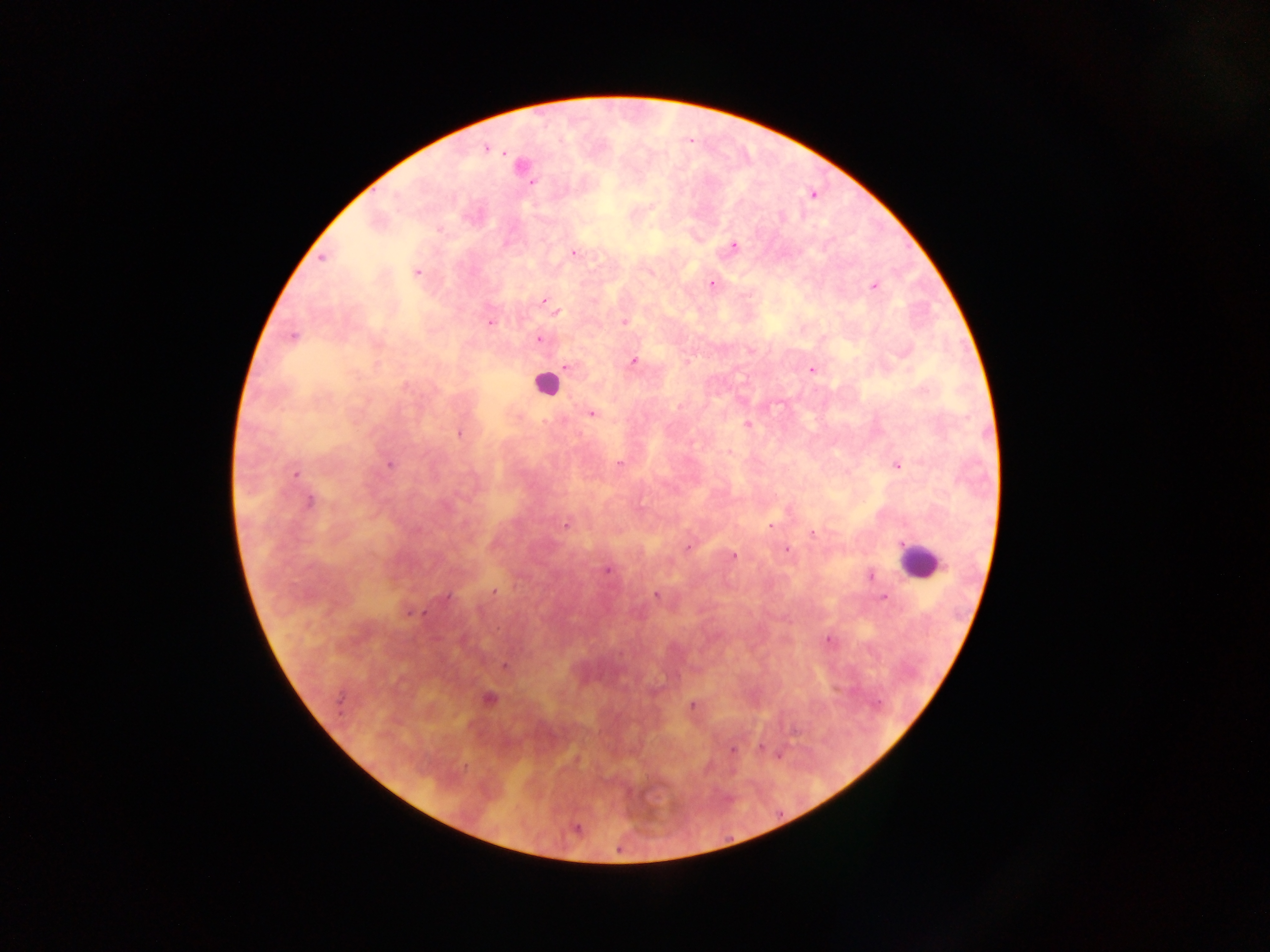 Approximate centers as [x, y] in pixels. Leukocyte locations: [545, 384], [919, 560]. Malaria parasite locations: [486, 148], [531, 182], [812, 195], [733, 246], [574, 253], [323, 258], [416, 272], [712, 284], [874, 287], [543, 301], [557, 313], [625, 321], [490, 322], [292, 336], [539, 340], [634, 361], [377, 364], [567, 366], [812, 370], [592, 414], [747, 425], [459, 434], [729, 452], [390, 464], [619, 464], [898, 465], [295, 474], [309, 502], [566, 524], [770, 525], [813, 533], [689, 547], [787, 549], [733, 555], [607, 570], [871, 576], [494, 591], [656, 595], [447, 596], [883, 597], [412, 612], [828, 640], [505, 666], [489, 699], [692, 705], [760, 747], [732, 751], [576, 828]. Thick blood smear. One field of view. Mobile-phone photograph taken through the microscope. Collected in Ghana. Image is 1270×952 pixels.